Classify this cell by malaria status.
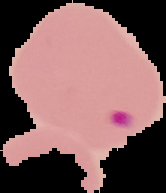
It is parasitized.

image type = segmented cell region with the area outside set to black
preparation = thin blood smear
image size = 166×193 pixels